Describe the morphology of the red blood cells.
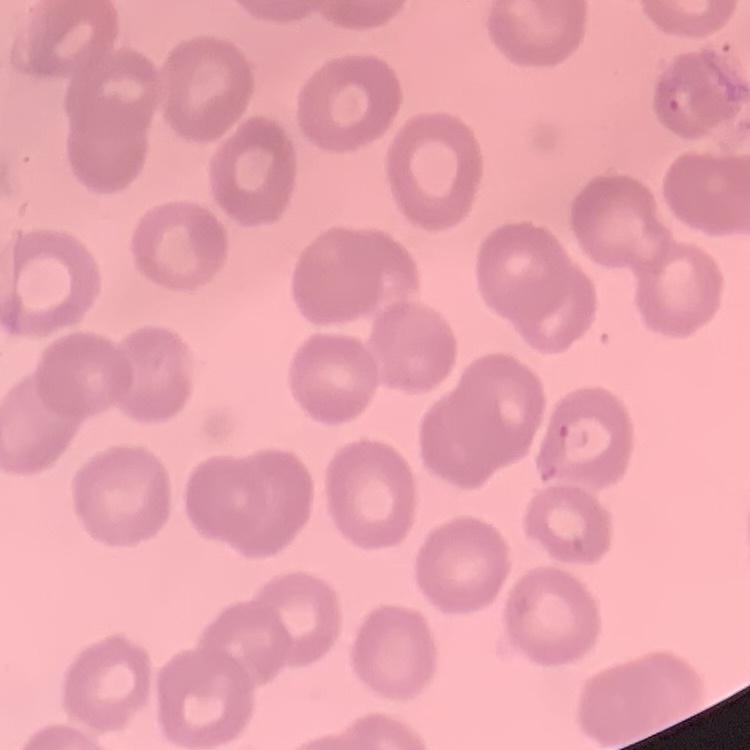
No rouleaux formation.

{
  "image_type": "one tile cut from a larger photomicrograph",
  "stain": "Field's or Giemsa",
  "preparation": "thin peripheral smear"
}